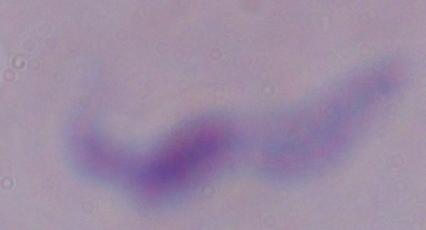
Summary:
  - Identification: trypanosome
  - Modality: photomicrograph
  - Magnification: 1000x